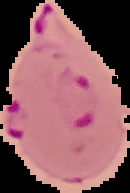
The area outside the segmented cell region is set to black. Image is 130×193 pixels. From a thin blood film. Malaria status: parasitized.